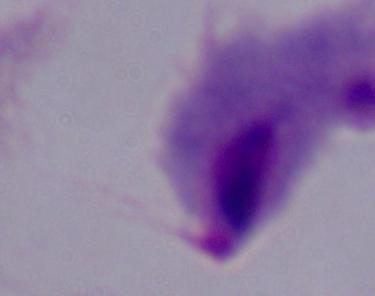
{
  "modality": "micrograph",
  "magnification": "1000x",
  "identification": "trichomonad"
}